Give the position of every Plasmodium parasite visible.
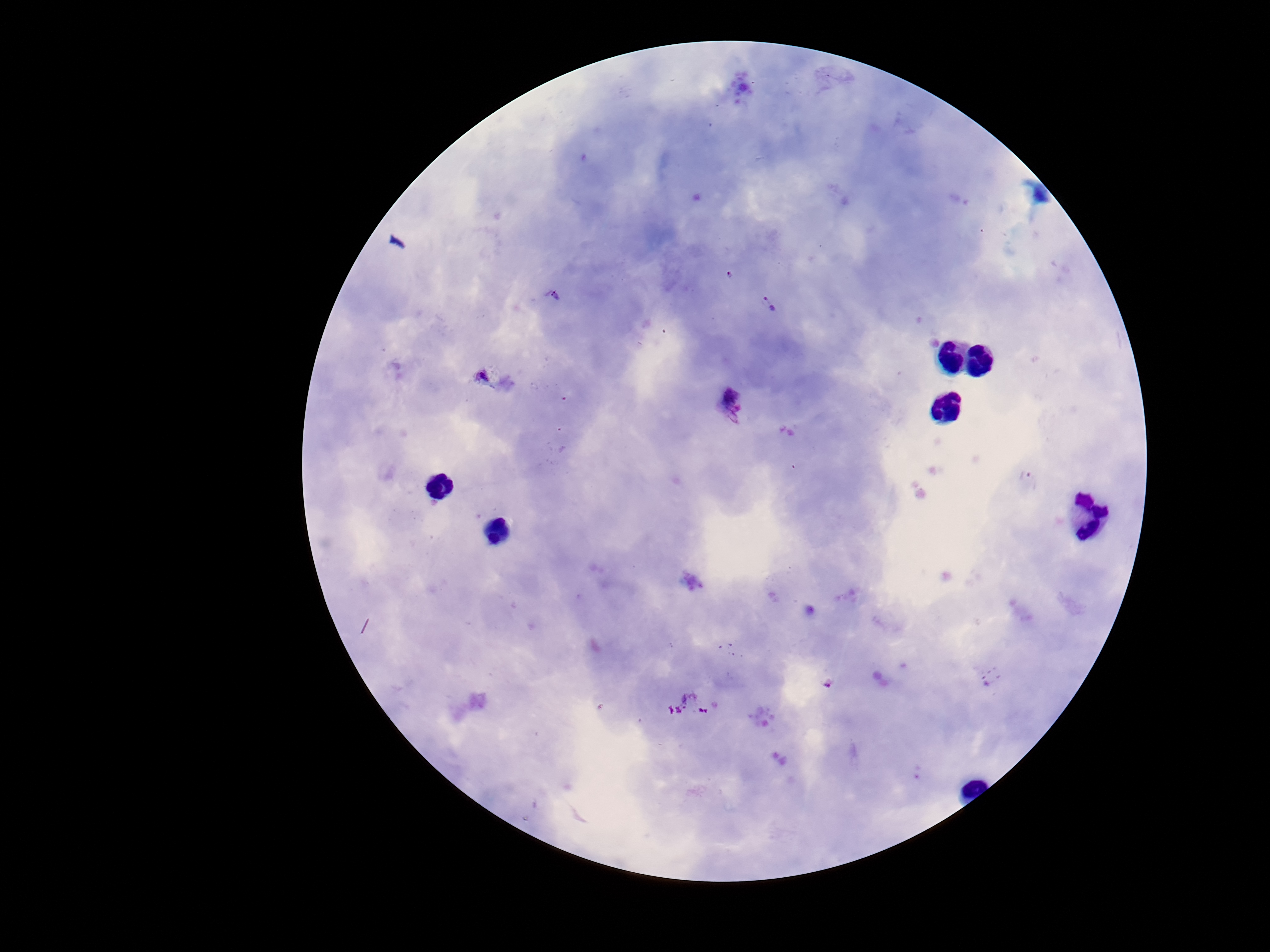

Approximate centers as [x, y] in pixels.
Plasmodium parasites: [769, 303], [481, 375], [733, 402], [828, 683].

Summary:
  - Stain: Giemsa
  - Image size: 1270×952 pixels
  - Field of view: single
  - Capture: smartphone camera through the microscope eyepiece
  - Preparation: thick blood smear
  - Patient malaria status: infected
  - Magnification: 100x